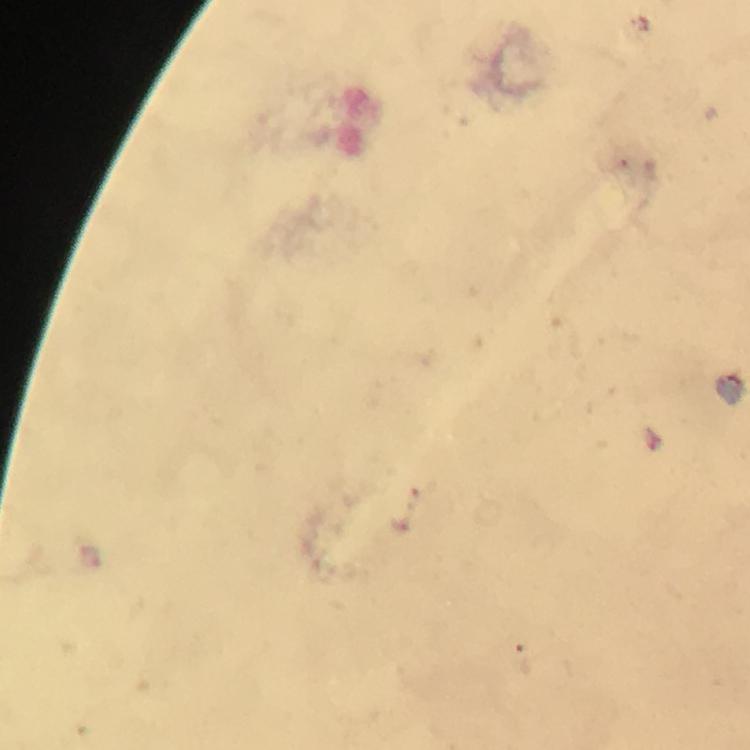
stain: Giemsa
capture: smartphone photograph through a microscope
context: from a malaria diagnostic workup
preparation: thick blood smear
magnification: 100x
cropped_from: one field of view
malaria_parasite_locations: 'approximate object centers, in pixels from the top-left corner: (x=91, y=553)'
immersion_oil: used
image_size: 750×750 pixels